Report the malaria status.
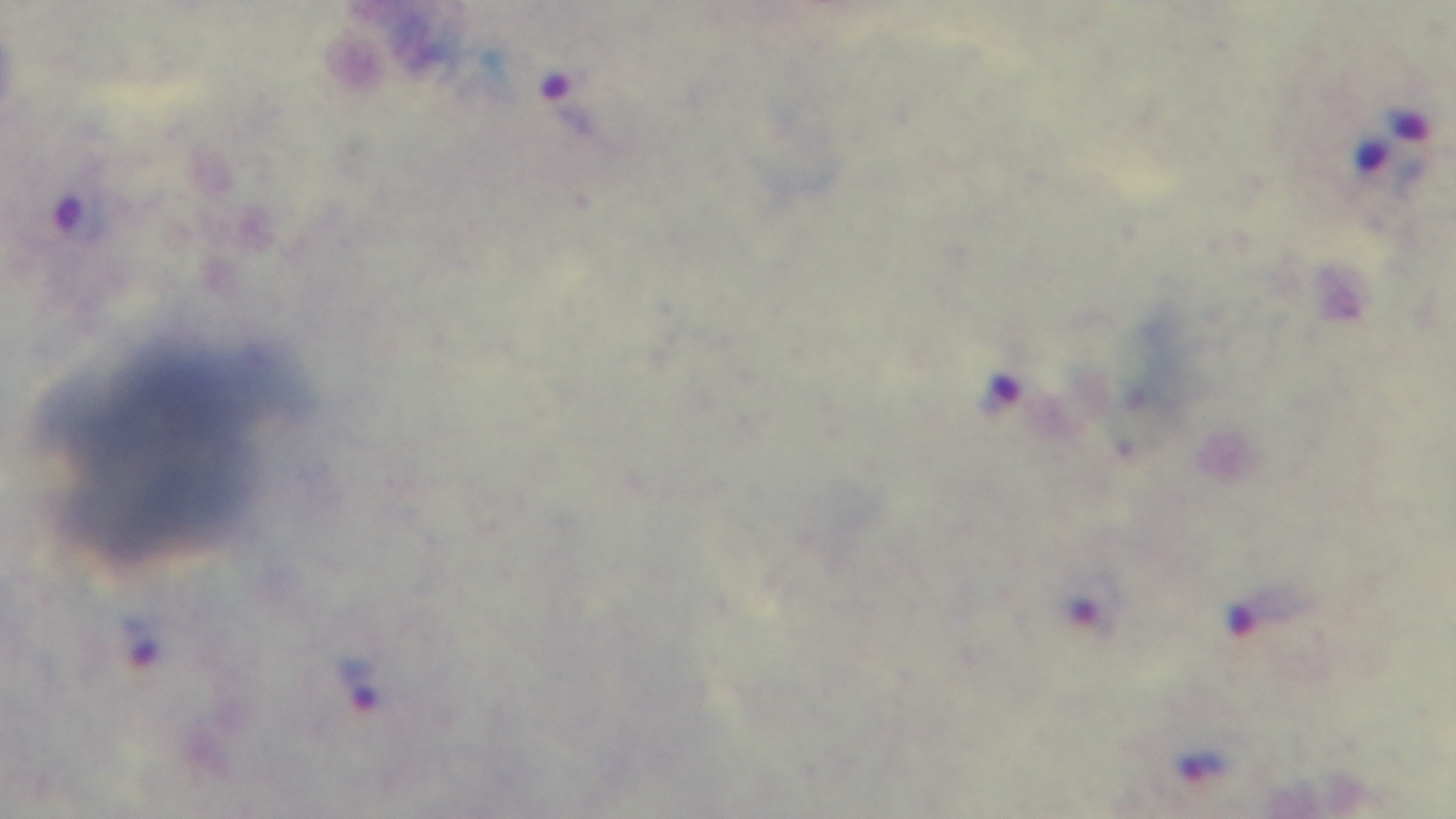

It is infected.

capture = mounted 4K digital camera
stain = Giemsa
field of view = single
modality = light microscopy
preparation = thick blood film
objective = 100x oil immersion